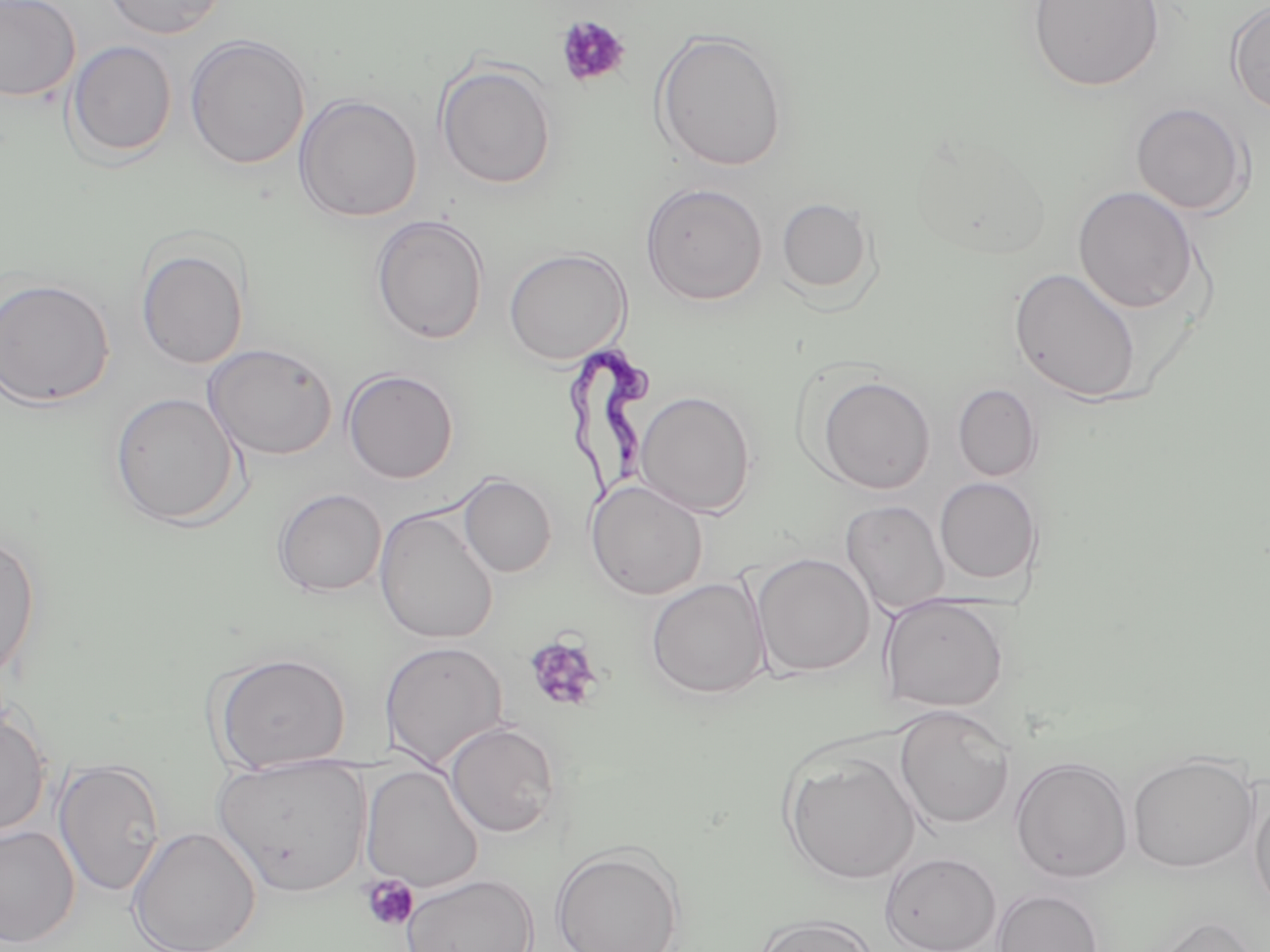
Summary:
  - Coordinate format: approximate bounding boxes as [x1, y1, x2, y2] in pixels
  - Platelet locations: [555, 15, 631, 88], [522, 633, 605, 714], [359, 875, 420, 932]
  - Uninfected red blood cell locations: [0, 0, 81, 102], [101, 0, 229, 38], [1027, 0, 1164, 92], [1226, 1, 1270, 116], [651, 28, 789, 173], [185, 34, 311, 170], [66, 40, 177, 161], [435, 60, 557, 189], [293, 93, 423, 222], [1130, 102, 1252, 216], [909, 132, 1054, 262], [640, 182, 768, 306], [1072, 185, 1200, 313], [776, 197, 875, 297], [370, 215, 489, 344], [136, 243, 250, 370], [504, 247, 631, 364], [1009, 267, 1143, 403], [0, 277, 115, 408], [203, 343, 338, 461], [342, 368, 459, 484], [815, 374, 935, 494], [953, 383, 1042, 481], [635, 390, 756, 517], [109, 392, 242, 528], [459, 473, 556, 578], [934, 477, 1042, 584], [585, 479, 708, 600], [272, 488, 387, 597], [840, 500, 950, 614], [374, 507, 498, 644], [0, 533, 41, 685], [751, 553, 875, 678], [646, 576, 770, 701], [879, 596, 1009, 713], [379, 640, 509, 770], [210, 651, 352, 772], [893, 705, 1015, 830], [0, 706, 51, 838], [444, 721, 562, 838], [781, 750, 920, 885], [1127, 752, 1259, 873], [213, 755, 372, 897], [1009, 756, 1133, 883], [53, 759, 166, 897], [360, 764, 483, 893], [1249, 782, 1270, 914], [0, 825, 80, 947], [127, 826, 261, 952], [551, 845, 684, 951], [880, 852, 1001, 952], [402, 873, 538, 952], [992, 888, 1103, 952], [753, 913, 881, 952], [1149, 914, 1262, 952]
  - Trypanosoma brucei locations: [558, 330, 660, 514]
  - Slide-level diagnosis: Trypanosoma brucei
  - Modality: light microscopy
  - Stain: May-Grünwald-Giemsa
  - Image size: 1270×952 pixels
  - Preparation: thin blood smear
  - Field of view: single
  - Magnification: 1000x